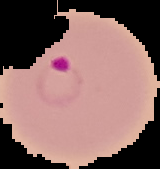 Cell region segmented out of the field of view; the surrounding area is masked to black. Image is 160×169 pixels. Malaria status: parasitized. From a thin blood film.